Report the malaria status of this cell.
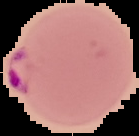
Parasitized.

Summary:
  - Preparation: thin blood film
  - Image size: 139×136 pixels
  - Image type: cell region segmented out of the field of view; surrounding area masked to black